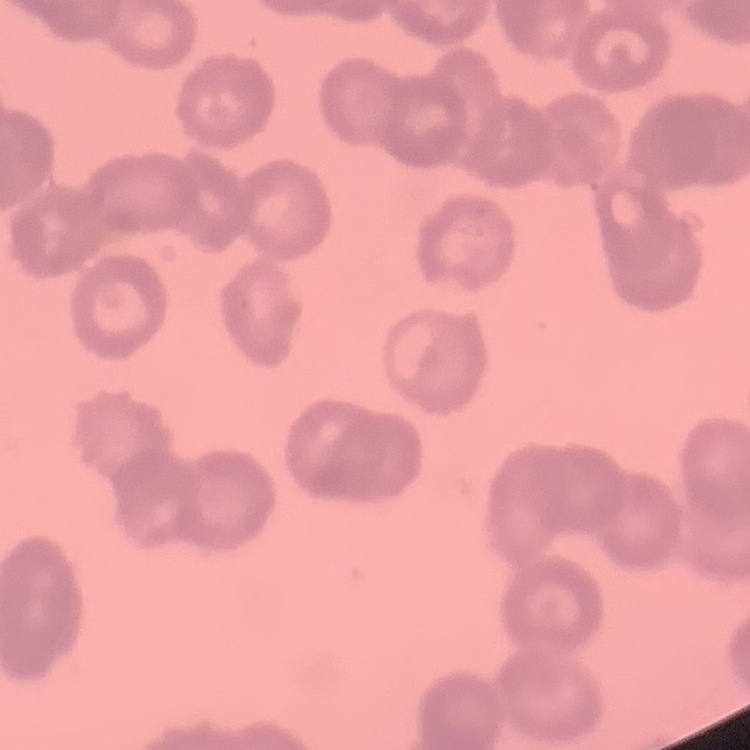 The erythrocytes exhibit rouleaux formation. Thin peripheral smear. Square crop of a larger photomicrograph. Stained with either Field's or Giemsa.